State which parasite is depicted.
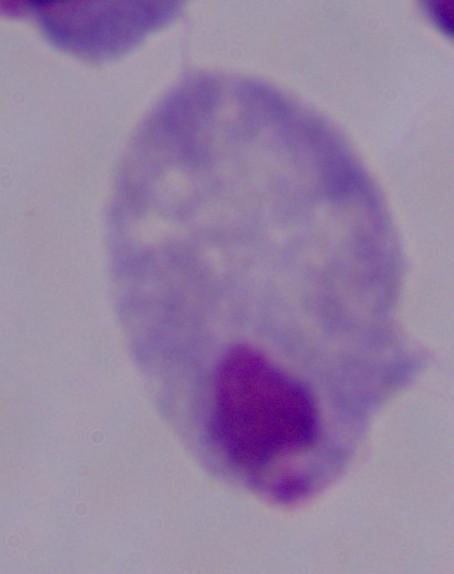

This is a trichomonad.

modality: micrograph
magnification: 1000x